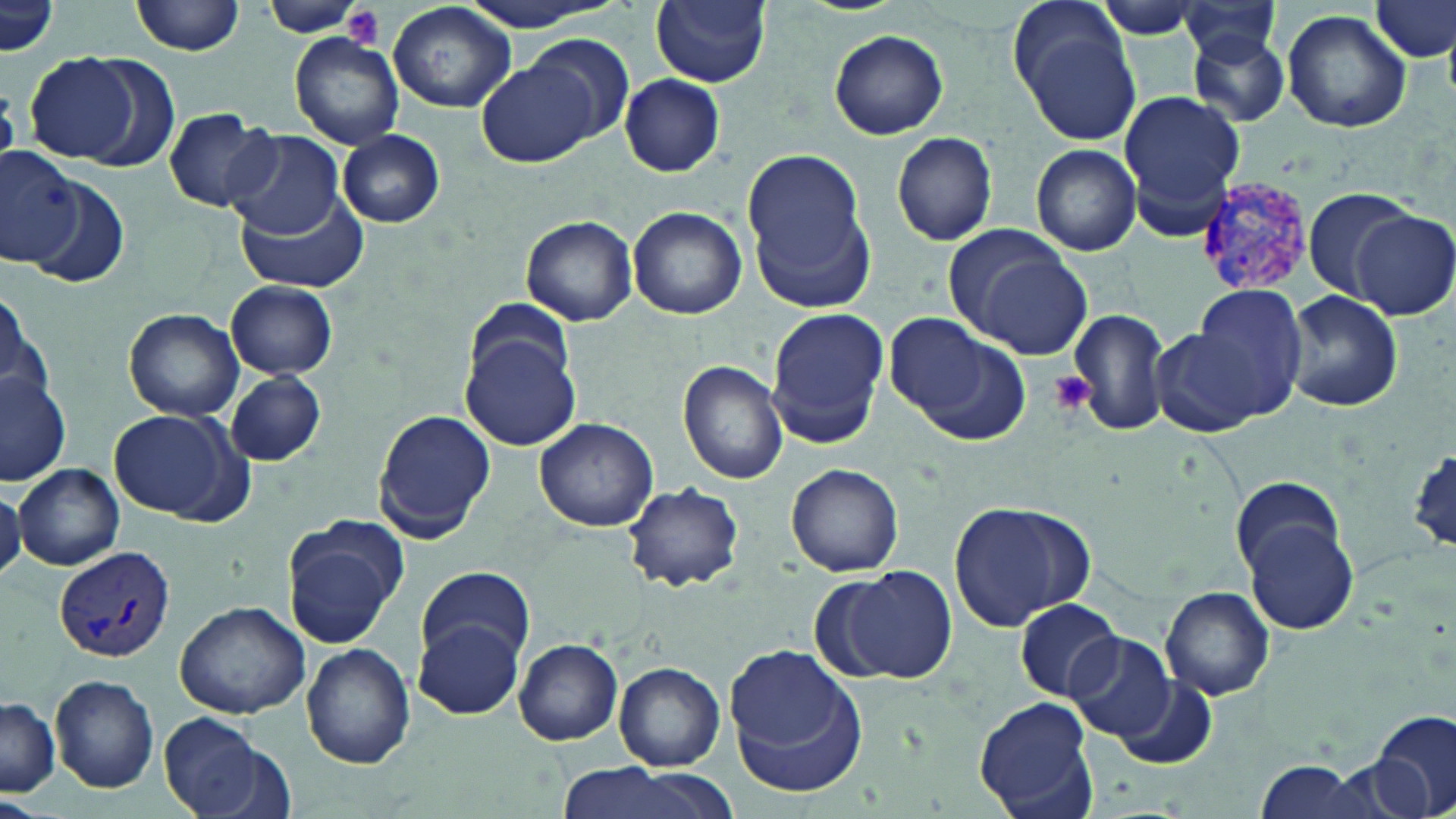

slide-level diagnosis = Plasmodium vivax
preparation = thin blood smear
field of view = one of a larger specimen
magnification = 1000x
image size = 1456×819 pixels
Plasmodium vivax-infected red blood cell locations = approximate bounding boxes as [x1, y1, x2, y2] in pixels: [1193, 176, 1320, 295], [54, 544, 178, 664]
stain = May-Grünwald-Giemsa
uninfected red blood cell locations = approximate bounding boxes as [x1, y1, x2, y2] in pixels: [132, 0, 247, 57], [454, 0, 624, 30], [1371, 0, 1455, 63], [652, 1, 771, 88], [1088, 1, 1211, 39], [266, 2, 370, 39], [388, 2, 517, 113], [1179, 2, 1284, 66], [1, 3, 58, 59], [1282, 9, 1411, 133], [1019, 19, 1143, 148], [1187, 28, 1291, 127], [828, 29, 948, 139], [289, 31, 406, 150], [523, 33, 636, 148], [24, 50, 158, 168], [479, 59, 601, 166], [620, 74, 725, 176], [1122, 91, 1243, 230], [160, 109, 279, 212], [225, 129, 342, 237], [338, 129, 446, 228], [891, 131, 999, 246], [1030, 143, 1141, 256], [741, 148, 875, 307], [0, 150, 82, 270], [25, 178, 131, 289], [235, 185, 367, 292], [1303, 186, 1417, 299], [626, 206, 747, 320], [1352, 210, 1456, 320], [520, 214, 638, 326], [947, 235, 1089, 354], [226, 281, 338, 378], [196, 284, 326, 440], [1192, 284, 1309, 414], [1, 286, 51, 421], [1282, 289, 1402, 413], [468, 296, 571, 391], [122, 307, 244, 421], [767, 308, 887, 436], [1067, 308, 1170, 435], [881, 313, 1022, 438], [1149, 325, 1270, 440], [461, 330, 580, 451], [679, 360, 789, 485], [1, 366, 71, 489], [225, 371, 325, 466], [107, 408, 249, 523], [373, 409, 495, 541], [533, 417, 658, 532], [1409, 449, 1456, 549], [785, 462, 904, 577], [13, 464, 124, 570], [1231, 475, 1345, 581], [624, 482, 745, 592], [0, 490, 24, 577], [949, 500, 1095, 632], [281, 514, 408, 648], [1243, 521, 1357, 635], [414, 565, 537, 666], [826, 565, 957, 684], [1161, 587, 1275, 701], [1013, 598, 1122, 702], [174, 600, 309, 719], [417, 619, 525, 721], [1065, 633, 1174, 743], [514, 639, 623, 745], [301, 643, 414, 769], [725, 648, 871, 798], [614, 661, 725, 769], [48, 673, 159, 794], [1114, 674, 1218, 768], [975, 695, 1098, 819], [1, 698, 59, 797], [158, 712, 267, 817], [1373, 712, 1455, 817], [1251, 762, 1370, 818], [550, 765, 731, 819], [0, 798, 51, 819]
modality = light microscopy
platelet locations = approximate bounding boxes as [x1, y1, x2, y2] in pixels: [339, 4, 383, 51], [1047, 370, 1095, 415]